Classify this cell by malaria status.
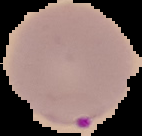
It is parasitized.

Summary:
  - Preparation: thin blood smear
  - Image size: 142×136 pixels
  - Image type: cell region segmented out of the field of view; surrounding area masked to black